Point out each leukocyte.
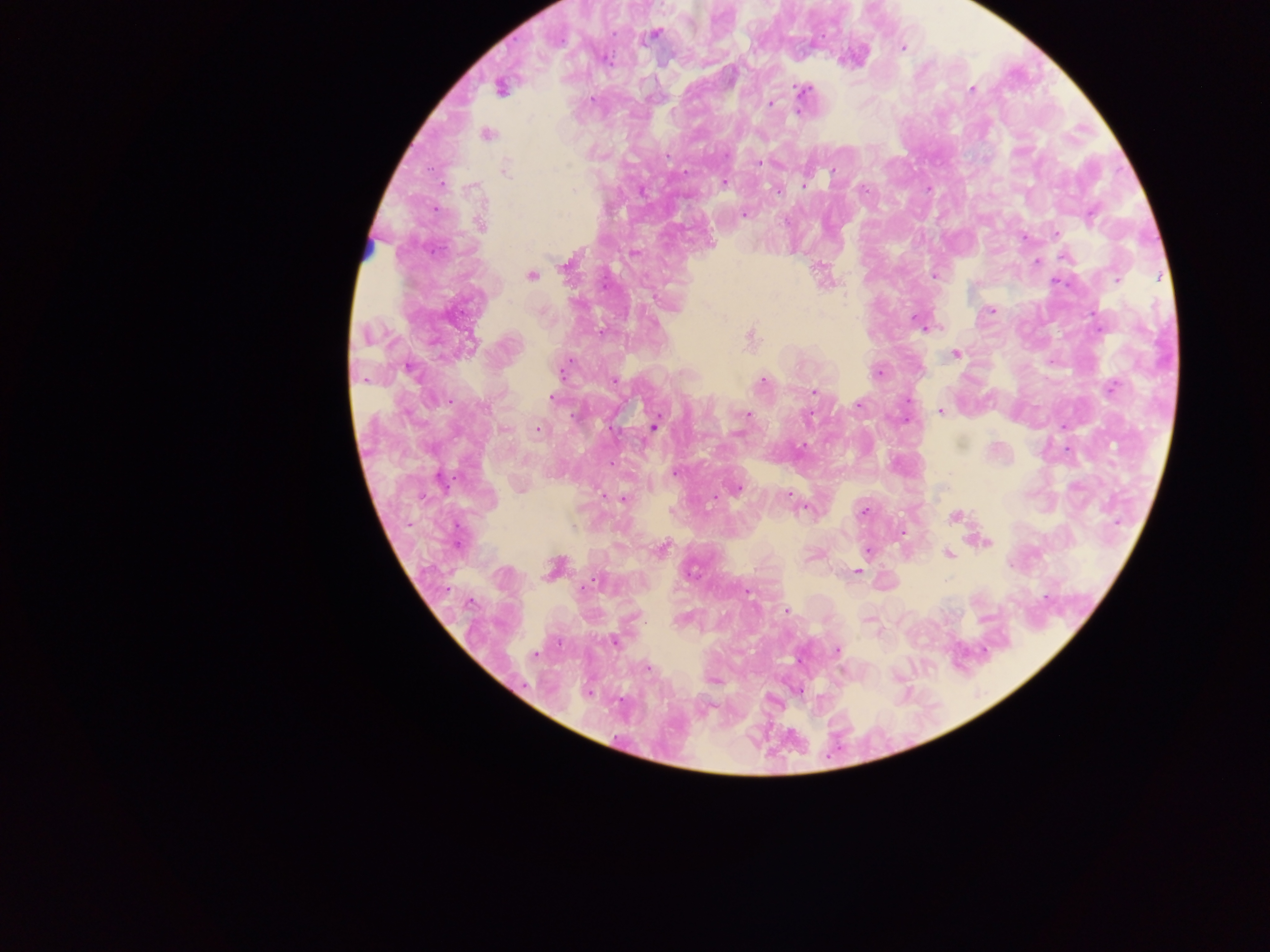
No leukocytes observed.

Approximate centers as (x, y) in pixels. Plasmodium parasite locations: (654, 34), (903, 47), (608, 61), (501, 88), (971, 89), (802, 91), (771, 103), (487, 134), (725, 154), (667, 157), (759, 163), (505, 169), (833, 171), (724, 183), (804, 185), (573, 190), (777, 190), (864, 190), (745, 214), (481, 224), (1056, 234), (711, 245), (634, 253), (1065, 257), (1036, 261), (569, 263), (531, 275), (935, 276), (1117, 278), (1058, 282), (991, 310), (915, 319), (751, 336), (956, 354), (564, 368), (410, 369), (878, 373), (614, 381), (762, 382), (1112, 388), (814, 392), (552, 397), (858, 404), (940, 412), (747, 415), (808, 418), (654, 426), (504, 429), (538, 429), (674, 473), (737, 489), (788, 495), (622, 499), (863, 511), (954, 517), (987, 542), (663, 549), (868, 551), (948, 554), (554, 568), (857, 572), (592, 584), (748, 594), (470, 602), (785, 611), (613, 641), (838, 650), (536, 655), (648, 667). Collected in Ghana. Photographed through a microscope with a mobile-phone camera. Thick blood smear. Single field of view. Image is 1270×952 pixels.